Outline each blood parasite and name the species.
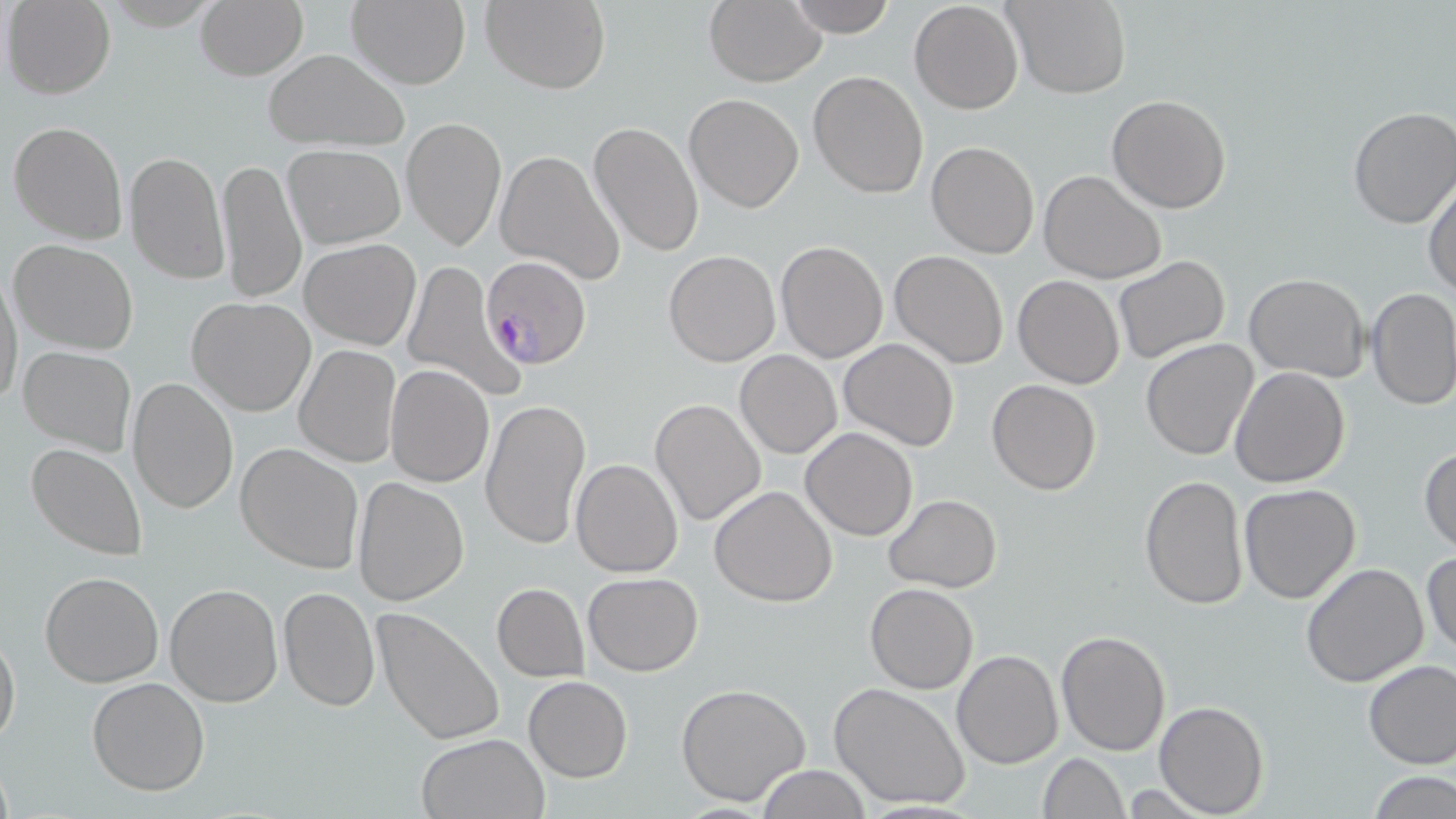
Approximate bounding boxes as [x1, y1, x2, y2] in pixels.
Plasmodium falciparum-infected red blood cells: [479, 255, 591, 370].
No Plasmodium ovale, Plasmodium malariae, Plasmodium vivax, Babesia divergens, or Trypanosoma brucei observed.

Summary:
  - Uninfected red blood cell locations: [194, 0, 308, 80], [347, 0, 472, 91], [480, 0, 610, 93], [703, 0, 826, 86], [784, 0, 897, 38], [1006, 0, 1130, 98], [4, 1, 115, 98], [908, 2, 1024, 115], [263, 49, 408, 153], [808, 70, 929, 197], [684, 94, 803, 212], [1106, 94, 1232, 214], [1347, 106, 1456, 229], [400, 117, 507, 253], [8, 119, 127, 245], [589, 120, 704, 257], [926, 140, 1038, 258], [282, 144, 406, 249], [494, 149, 625, 285], [124, 150, 230, 284], [217, 156, 308, 307], [1038, 169, 1167, 283], [1423, 175, 1456, 299], [299, 238, 421, 351], [8, 239, 138, 355], [774, 240, 889, 364], [664, 249, 781, 366], [888, 250, 1010, 368], [1113, 255, 1231, 366], [401, 260, 526, 405], [0, 266, 21, 415], [1243, 273, 1368, 382], [1012, 275, 1124, 388], [1365, 286, 1456, 410], [186, 297, 316, 417], [839, 338, 960, 453], [1140, 338, 1258, 461], [17, 345, 136, 456], [294, 345, 401, 467], [735, 350, 842, 458], [385, 364, 495, 487], [1230, 366, 1351, 489], [127, 377, 239, 516], [986, 379, 1101, 494], [479, 397, 592, 551], [650, 398, 766, 527], [800, 427, 918, 540], [235, 443, 363, 574], [25, 444, 148, 562], [1419, 445, 1455, 556], [570, 457, 684, 576], [1137, 476, 1250, 610], [352, 478, 470, 606], [1239, 483, 1362, 603], [710, 485, 838, 606], [884, 494, 1001, 593], [1422, 549, 1455, 660], [1301, 561, 1430, 686], [40, 572, 165, 688], [583, 572, 703, 675], [164, 583, 283, 707], [492, 583, 589, 683], [866, 583, 977, 693], [277, 586, 380, 712], [372, 606, 505, 749], [1056, 630, 1172, 755], [0, 632, 21, 748], [952, 649, 1062, 767], [1362, 658, 1456, 769], [86, 676, 210, 797], [524, 676, 632, 783], [677, 681, 811, 807], [829, 682, 970, 810], [1153, 700, 1269, 817], [415, 732, 549, 818], [1039, 753, 1127, 817], [757, 764, 872, 819], [1369, 771, 1454, 818], [1117, 784, 1216, 818]
  - Slide-level diagnosis: Plasmodium falciparum
  - Stain: May-Grünwald-Giemsa
  - Preparation: thin blood film
  - Modality: optical microscopy
  - Image size: 1456×819 pixels
  - Field of view: single
  - Magnification: 1000x